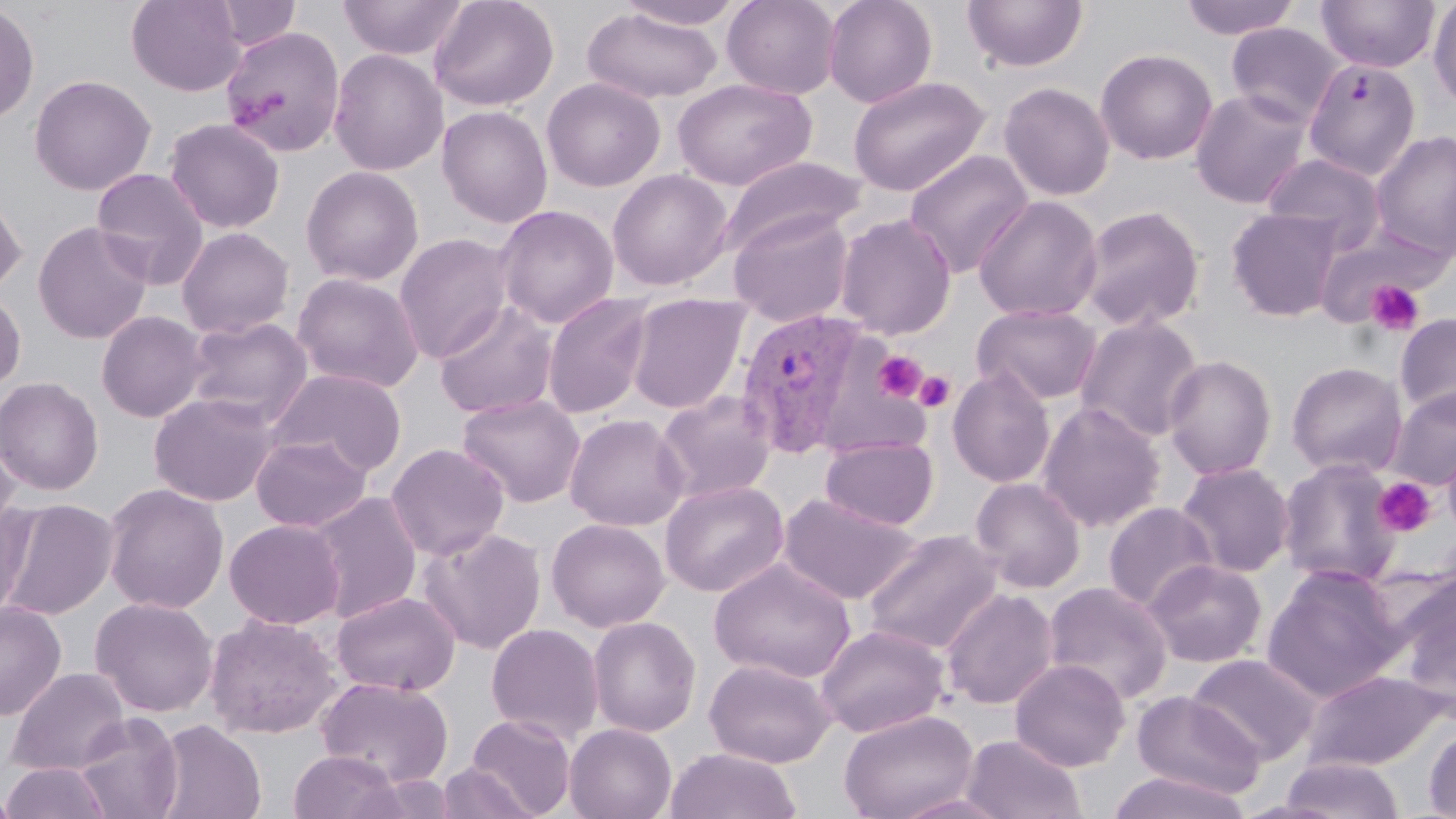

Summary:
  - Coordinate format: approximate bounding boxes as [x1, y1, x2, y2] in pixels
  - Plasmodium vivax-infected red blood cell locations: [734, 307, 872, 459]
  - Uninfected red blood cell locations: [126, 0, 248, 96], [336, 0, 543, 89], [338, 0, 469, 60], [429, 0, 559, 111], [616, 0, 746, 29], [722, 0, 841, 99], [822, 0, 938, 108], [962, 0, 1088, 73], [1178, 0, 1303, 40], [1315, 0, 1440, 74], [211, 1, 301, 51], [1427, 2, 1456, 108], [0, 3, 40, 125], [583, 8, 722, 103], [1225, 22, 1344, 127], [220, 25, 346, 158], [1095, 48, 1218, 165], [328, 49, 448, 176], [1303, 58, 1421, 180], [29, 74, 156, 196], [847, 75, 991, 197], [541, 77, 665, 192], [673, 77, 817, 190], [998, 81, 1115, 201], [1190, 88, 1313, 209], [437, 105, 553, 228], [163, 118, 286, 234], [1370, 129, 1456, 260], [904, 149, 1034, 277], [1262, 152, 1387, 254], [718, 155, 866, 256], [300, 165, 424, 286], [90, 167, 211, 289], [606, 168, 734, 291], [0, 185, 27, 297], [973, 195, 1103, 322], [494, 205, 619, 328], [1076, 205, 1205, 332], [1226, 207, 1343, 322], [728, 208, 854, 326], [834, 213, 956, 339], [32, 221, 154, 344], [176, 227, 295, 339], [394, 233, 514, 363], [292, 273, 424, 393], [0, 288, 26, 393], [542, 292, 654, 418], [626, 293, 750, 414], [433, 301, 559, 419], [971, 303, 1102, 406], [96, 311, 210, 423], [1394, 312, 1456, 419], [1074, 314, 1204, 443], [184, 316, 311, 427], [1162, 354, 1278, 481], [1286, 361, 1408, 478], [268, 368, 409, 475], [947, 368, 1056, 488], [0, 376, 104, 496], [1387, 386, 1456, 490], [655, 390, 778, 503], [148, 391, 282, 506], [457, 393, 586, 508], [1037, 401, 1165, 532], [563, 413, 689, 531], [0, 431, 22, 542], [250, 433, 372, 533], [820, 436, 939, 530], [1442, 440, 1456, 538], [385, 443, 509, 561], [1277, 457, 1403, 588], [1175, 462, 1294, 578], [970, 476, 1086, 592], [659, 480, 788, 597], [102, 483, 229, 614], [309, 491, 423, 623], [779, 492, 922, 605], [0, 498, 35, 622], [0, 499, 119, 620], [1103, 502, 1218, 613], [546, 518, 669, 632], [224, 519, 346, 630], [418, 526, 547, 654], [862, 529, 1004, 657], [709, 558, 855, 683], [1144, 560, 1267, 667], [1261, 565, 1407, 703], [1392, 575, 1456, 720], [1042, 581, 1173, 705], [941, 588, 1059, 710], [331, 591, 461, 696], [90, 597, 218, 717], [0, 600, 66, 721], [204, 614, 342, 739], [587, 616, 701, 737], [486, 623, 604, 743], [816, 624, 950, 737], [1188, 654, 1321, 765], [705, 658, 835, 768], [1011, 658, 1129, 771], [6, 667, 131, 776], [1300, 670, 1449, 772], [316, 676, 453, 788], [1131, 691, 1266, 800], [839, 709, 980, 819], [74, 712, 183, 819], [466, 714, 576, 818], [151, 719, 266, 819], [564, 723, 677, 819], [1423, 724, 1456, 818], [961, 735, 1087, 819], [665, 747, 802, 819], [288, 750, 403, 819], [1279, 757, 1404, 818], [1, 761, 114, 819], [435, 762, 539, 819], [1106, 771, 1253, 819], [353, 773, 461, 818], [0, 784, 21, 819], [892, 792, 1017, 818]
  - Platelet locations: [1365, 280, 1425, 336], [873, 351, 927, 402], [913, 371, 956, 413], [1373, 477, 1437, 538]
  - Slide-level diagnosis: Plasmodium vivax
  - Preparation: thin blood smear
  - Modality: light microscopy
  - Image size: 1456×819 pixels
  - Magnification: 1000x
  - Field of view: single
  - Stain: May-Grünwald-Giemsa